State the blood parasite species.
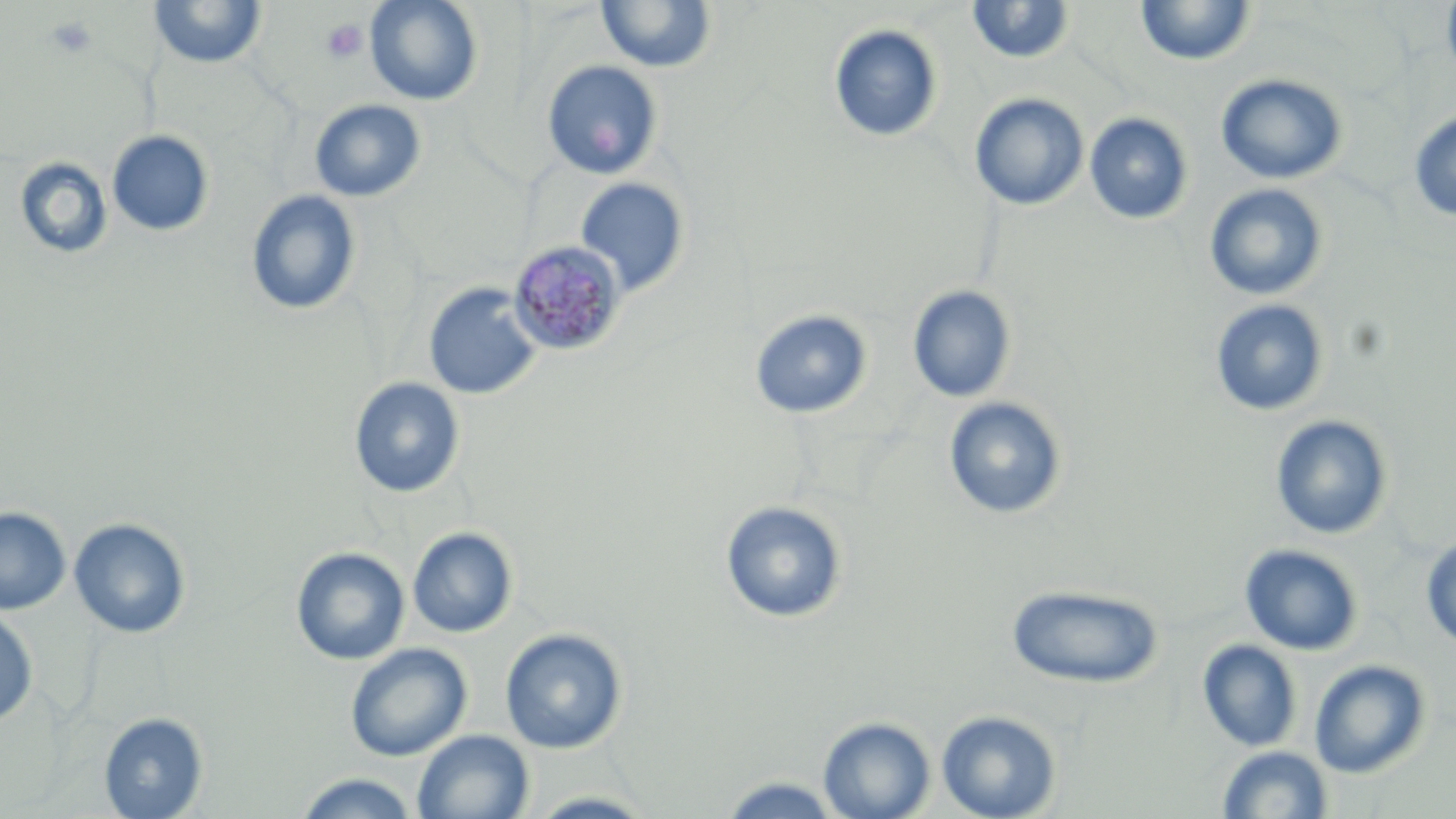

Plasmodium malariae.

Approximate bounding boxes as [x1, y1, x2, y2] in pixels. Uninfected red blood cell locations: [364, 0, 484, 106], [1440, 0, 1456, 89], [148, 1, 268, 71], [595, 1, 718, 73], [966, 1, 1076, 66], [1135, 1, 1256, 67], [828, 24, 943, 144], [540, 60, 664, 180], [1215, 73, 1348, 185], [969, 93, 1090, 211], [309, 98, 427, 202], [1408, 109, 1456, 222], [1084, 112, 1193, 225], [107, 130, 214, 237], [13, 157, 113, 261], [574, 177, 690, 296], [1203, 183, 1329, 301], [245, 190, 362, 317], [423, 283, 542, 400], [907, 285, 1017, 403], [1210, 299, 1330, 416], [749, 309, 873, 419], [349, 377, 466, 498], [943, 396, 1068, 520], [1269, 414, 1394, 539], [720, 500, 848, 624], [0, 507, 71, 615], [69, 517, 191, 639], [407, 527, 518, 638], [1420, 534, 1456, 652], [1239, 543, 1364, 656], [290, 547, 409, 666], [1005, 583, 1165, 689], [0, 608, 39, 726], [499, 628, 628, 754], [1197, 639, 1303, 752], [345, 642, 471, 761], [1308, 659, 1432, 779], [936, 709, 1062, 819], [99, 712, 208, 818], [817, 715, 936, 819], [413, 730, 534, 819], [1216, 745, 1334, 818], [293, 772, 422, 818], [713, 774, 848, 817], [523, 789, 660, 818]. Platelet locations: [45, 14, 99, 59], [321, 19, 368, 64]. Plasmodium malariae-infected red blood cell locations: [507, 239, 627, 357]. One field of a larger specimen. Optical microscopy. Image is 1456×819 pixels. Captured at 1000x magnification. May-Grünwald-Giemsa-stained preparation. Thin blood smear.